Locate every Plasmodium falciparum parasite and identify its life-cycle stage.
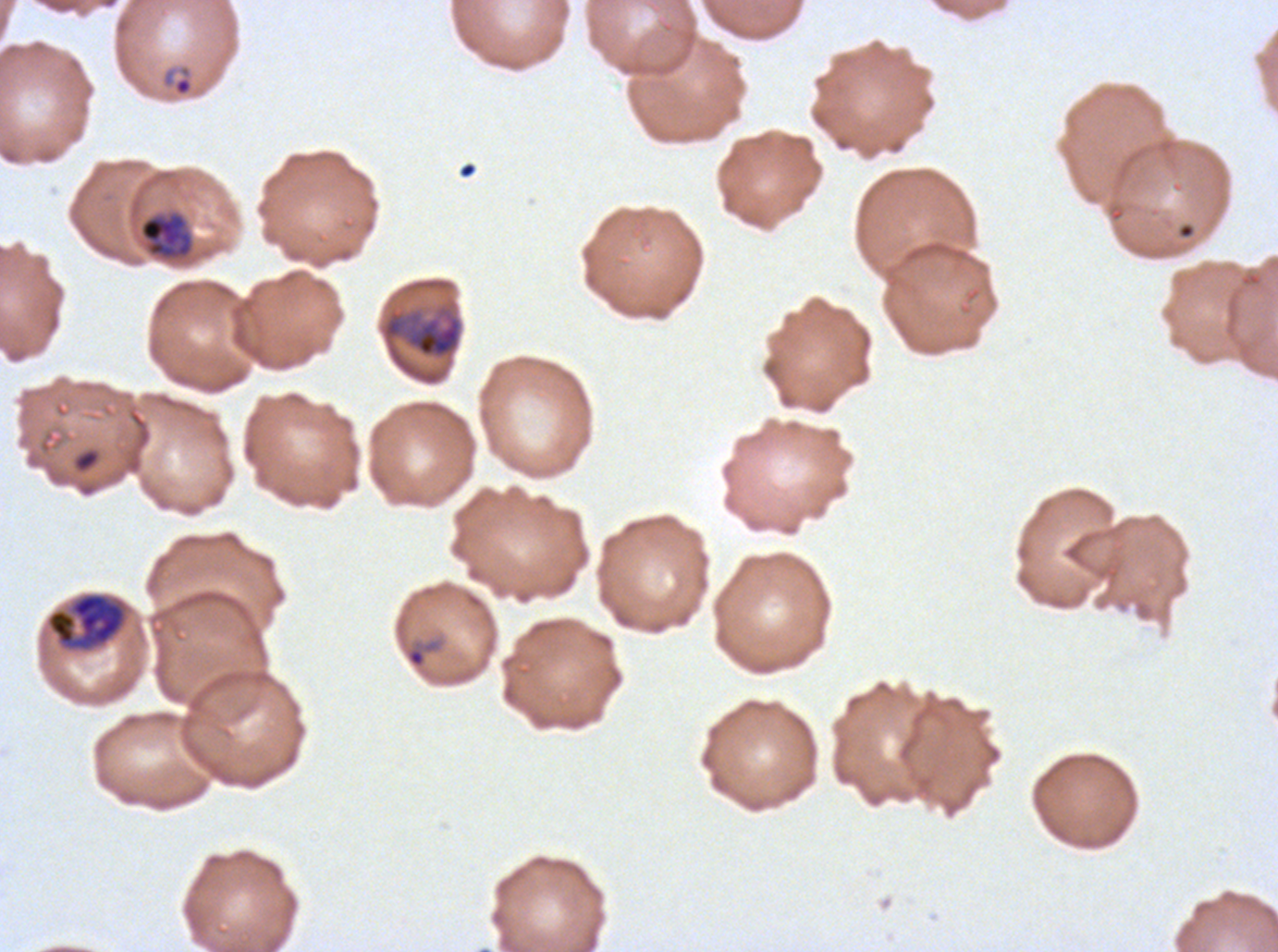
Approximate bounding rectangles given as corner coordinates in pixels from the top-left.
Rings: (x1=160, y1=64, x2=194, y2=98), (x1=404, y1=638, x2=442, y2=670).
Mid trophozoites: (x1=139, y1=212, x2=193, y2=260).
Late trophozoites: (x1=381, y1=306, x2=462, y2=360), (x1=45, y1=592, x2=128, y2=653).
No late-ring/early-trophozoite forms, early schizonts, late schizonts, segmenters, or gametocytes observed.

debris locations = (x1=1177, y1=223, x2=1195, y2=239), (x1=71, y1=446, x2=102, y2=474)
image size = 1278×952 pixels
stain = Giemsa
specimen = Plasmodium falciparum from a patient in The Gambia, cultured ex vivo for 24 to 48 hours
life-cycle stages observed = ring, mid trophozoite, late trophozoite
field of view = sub-image separated from a larger composite
preparation = thin blood smear